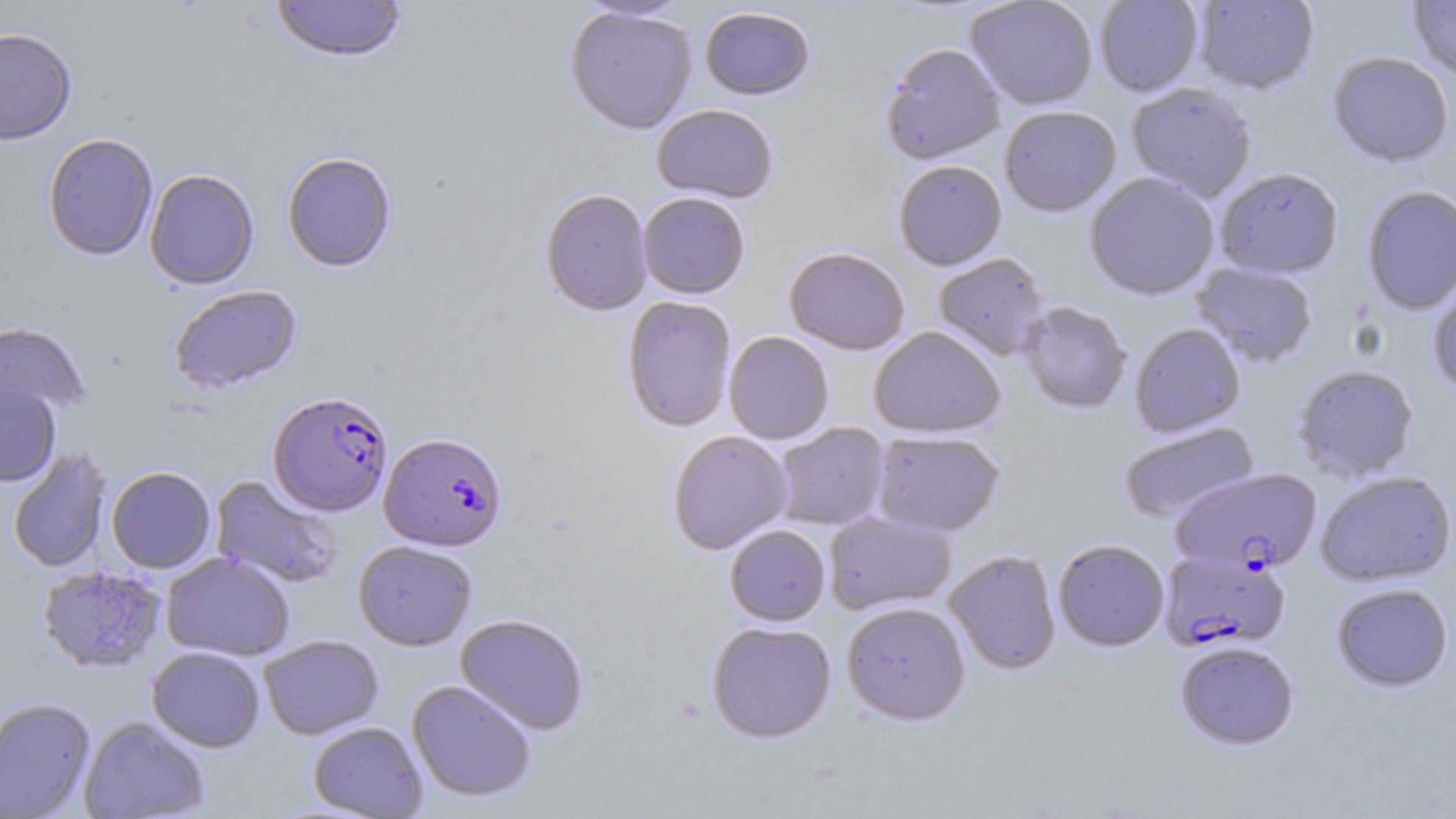

Summary:
  - Coordinate format: approximate bounding boxes as named x1/y1/x2/y2 corners in pixels
  - Plasmodium falciparum-infected red blood cell locations: (x1=268, y1=391, x2=393, y2=517), (x1=379, y1=432, x2=507, y2=552), (x1=1171, y1=468, x2=1323, y2=576), (x1=1159, y1=550, x2=1291, y2=653)
  - Uninfected red blood cell locations: (x1=271, y1=0, x2=407, y2=65), (x1=573, y1=0, x2=693, y2=22), (x1=965, y1=0, x2=1099, y2=111), (x1=1095, y1=0, x2=1204, y2=98), (x1=1192, y1=0, x2=1320, y2=97), (x1=1407, y1=1, x2=1456, y2=81), (x1=564, y1=6, x2=697, y2=136), (x1=699, y1=8, x2=815, y2=102), (x1=0, y1=28, x2=77, y2=146), (x1=880, y1=45, x2=1006, y2=166), (x1=1326, y1=53, x2=1454, y2=170), (x1=1126, y1=83, x2=1257, y2=203), (x1=651, y1=106, x2=778, y2=205), (x1=1000, y1=107, x2=1121, y2=218), (x1=42, y1=134, x2=158, y2=262), (x1=281, y1=153, x2=397, y2=273), (x1=893, y1=162, x2=1007, y2=272), (x1=145, y1=170, x2=259, y2=290), (x1=1215, y1=170, x2=1344, y2=282), (x1=1084, y1=173, x2=1220, y2=301), (x1=1362, y1=187, x2=1456, y2=316), (x1=539, y1=190, x2=652, y2=317), (x1=638, y1=194, x2=750, y2=300), (x1=783, y1=248, x2=910, y2=357), (x1=933, y1=253, x2=1050, y2=361), (x1=1192, y1=263, x2=1318, y2=368), (x1=1427, y1=276, x2=1456, y2=399), (x1=169, y1=285, x2=302, y2=395), (x1=622, y1=296, x2=737, y2=433), (x1=1019, y1=302, x2=1131, y2=415), (x1=0, y1=322, x2=91, y2=419), (x1=1129, y1=324, x2=1246, y2=437), (x1=868, y1=327, x2=1006, y2=438), (x1=723, y1=332, x2=834, y2=445), (x1=1292, y1=365, x2=1419, y2=482), (x1=0, y1=381, x2=61, y2=487), (x1=772, y1=422, x2=890, y2=531), (x1=1118, y1=422, x2=1260, y2=524), (x1=667, y1=431, x2=793, y2=555), (x1=871, y1=431, x2=1006, y2=538), (x1=7, y1=446, x2=113, y2=573), (x1=106, y1=467, x2=216, y2=574), (x1=1315, y1=471, x2=1455, y2=588), (x1=209, y1=474, x2=344, y2=590), (x1=824, y1=511, x2=956, y2=615), (x1=724, y1=525, x2=831, y2=627), (x1=1053, y1=539, x2=1169, y2=652), (x1=353, y1=541, x2=477, y2=652), (x1=944, y1=550, x2=1062, y2=676), (x1=161, y1=552, x2=295, y2=661), (x1=35, y1=565, x2=168, y2=673), (x1=1330, y1=583, x2=1454, y2=694), (x1=841, y1=601, x2=971, y2=726), (x1=455, y1=613, x2=590, y2=736), (x1=706, y1=621, x2=836, y2=744), (x1=259, y1=635, x2=384, y2=740), (x1=1174, y1=641, x2=1300, y2=751), (x1=147, y1=646, x2=265, y2=753), (x1=406, y1=679, x2=537, y2=803), (x1=0, y1=697, x2=96, y2=818), (x1=78, y1=715, x2=211, y2=819), (x1=308, y1=721, x2=428, y2=818)
  - Slide-level diagnosis: Plasmodium falciparum
  - Magnification: 1000x
  - Modality: light microscopy
  - Field of view: single
  - Preparation: thin blood smear
  - Stain: May-Grünwald-Giemsa
  - Image size: 1456×819 pixels